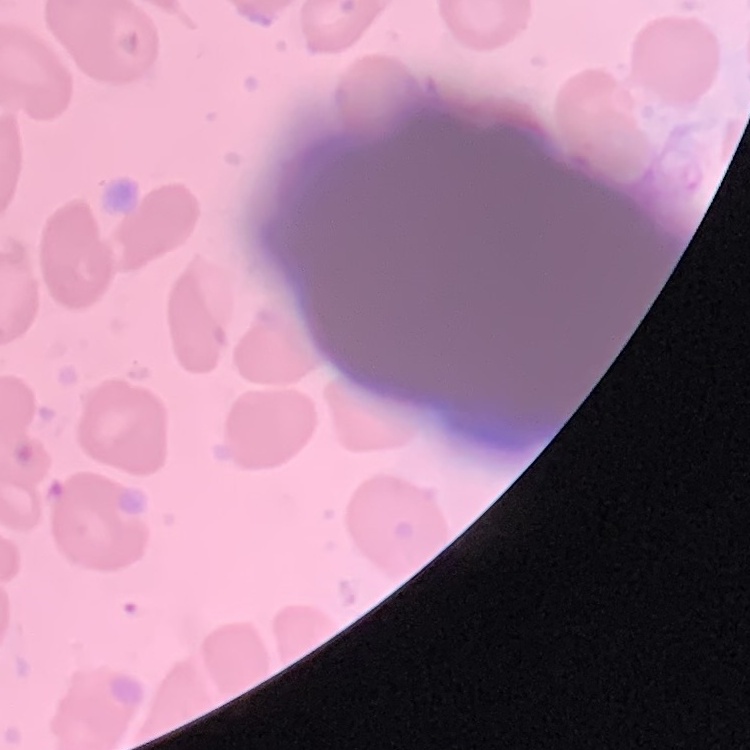
The red blood cells show no rouleaux formation. Stained with either Field's or Giemsa. Square crop of a larger photomicrograph. Thin blood film.